State the preparation type.
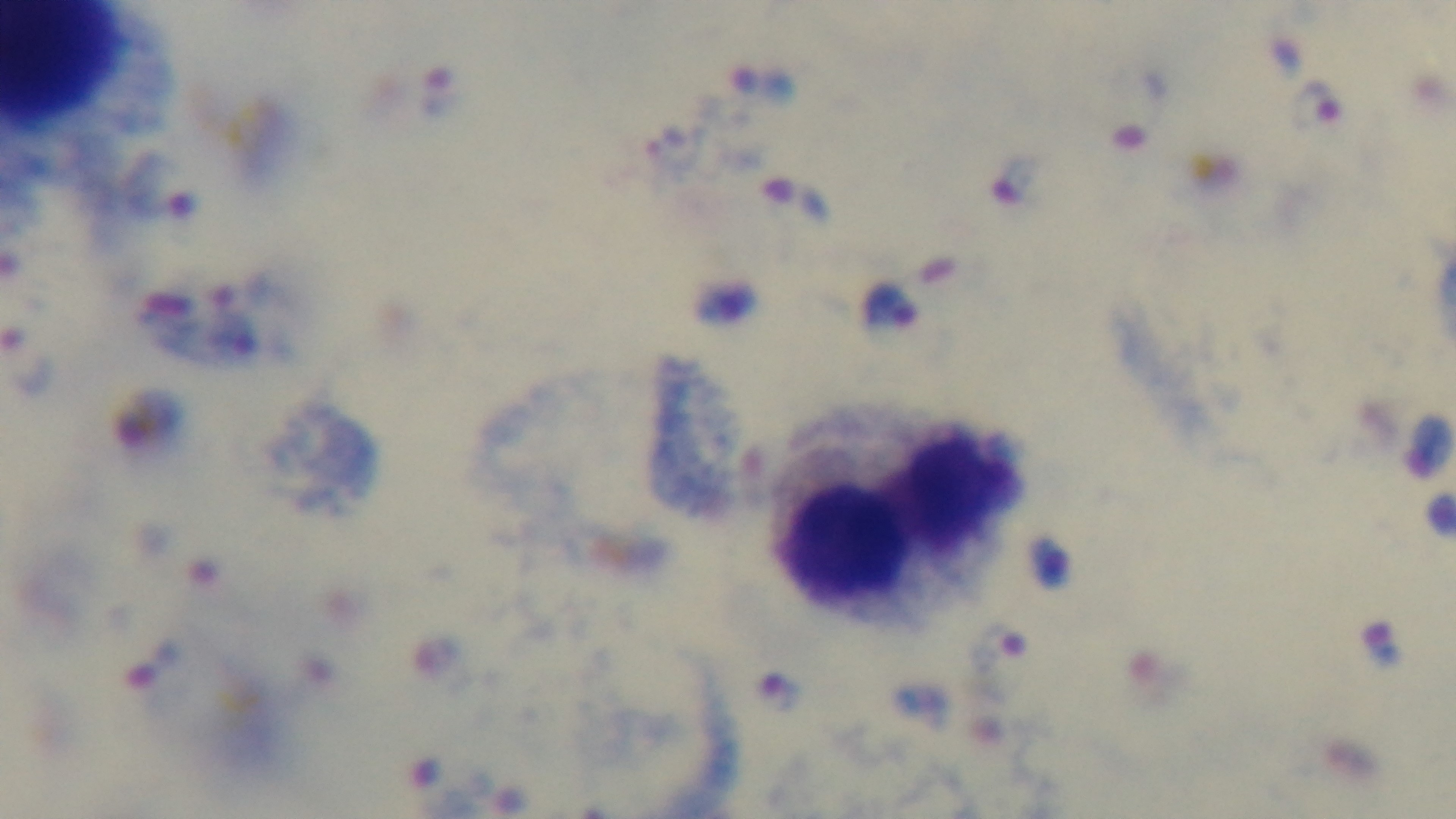
A thick smear.

stain = Giemsa
capture = mounted 4K digital camera
modality = light microscopy
objective = 100x oil immersion
field of view = single
malaria status = infected